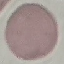
Summary:
  - Result: negative for malaria parasites
  - Preparation: thin blood smear
  - Stain: Giemsa
  - Image type: cell patch, automatically extracted from a larger field of view and resized to 64 × 64 pixels
  - Capture: smartphone through the microscope eyepiece